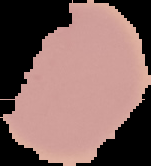
result = no Plasmodium parasites detected
image type = segmented cell region on a black background
preparation = thin blood film
image size = 151×166 pixels